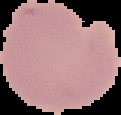

image_type: cell region segmented out of the field of view; surrounding area masked to black
malaria_status: uninfected
preparation: thin blood smear
image_size: 121×115 pixels